Assess this cell for malaria.
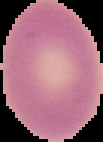
It is uninfected.

Summary:
  - Image size: 103×142 pixels
  - Image type: segmented cell region on a black background
  - Preparation: thin blood smear